Assess this cell for malaria.
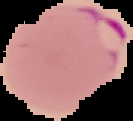
Parasitized.

Summary:
  - Image size: 133×121 pixels
  - Preparation: thin blood smear
  - Image type: segmented cell region on a black background